Locate every blood parasite and identify its species.
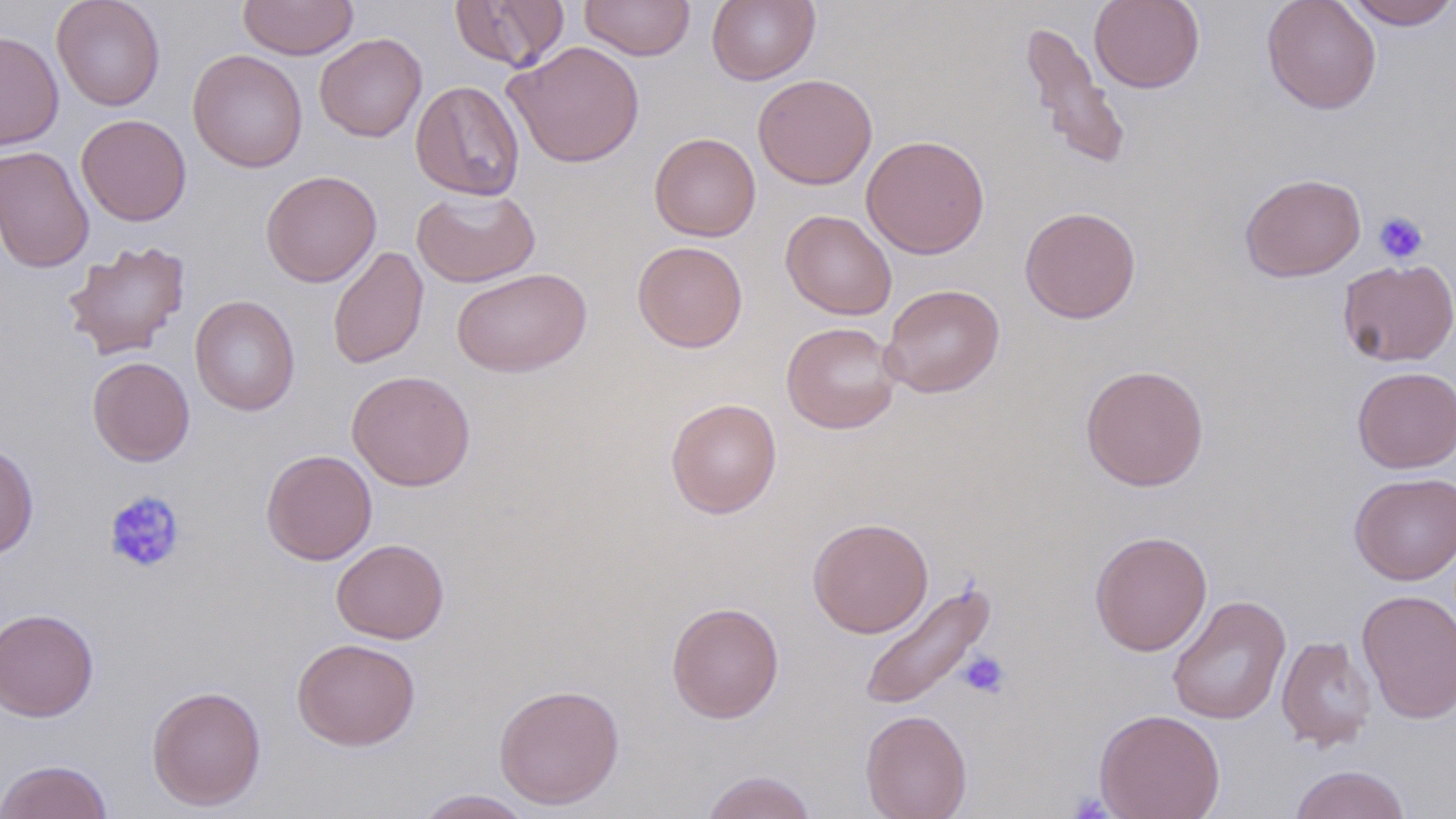
No blood parasites seen.

Summary:
  - Coordinate format: approximate bounding boxes as [x1, y1, x2, y2] in pixels
  - Platelet locations: [1373, 211, 1429, 264], [104, 490, 186, 574], [957, 650, 1011, 699], [1068, 791, 1116, 818]
  - Uninfected red blood cell locations: [51, 0, 166, 111], [238, 0, 358, 60], [449, 0, 571, 72], [579, 0, 695, 61], [706, 0, 820, 85], [1089, 0, 1205, 93], [1261, 0, 1382, 114], [1344, 0, 1456, 30], [1019, 20, 1132, 173], [0, 30, 64, 151], [314, 32, 427, 142], [505, 41, 645, 168], [187, 49, 307, 172], [752, 73, 877, 189], [410, 80, 525, 201], [76, 114, 192, 226], [649, 132, 761, 242], [861, 135, 989, 259], [0, 145, 94, 273], [260, 170, 381, 287], [1239, 173, 1366, 282], [411, 186, 541, 288], [1019, 206, 1141, 324], [781, 209, 897, 320], [62, 240, 191, 361], [632, 240, 748, 352], [328, 247, 429, 370], [1338, 258, 1456, 366], [452, 268, 591, 378], [880, 284, 1005, 398], [189, 295, 301, 416], [781, 321, 902, 434], [87, 356, 195, 466], [1080, 363, 1209, 491], [1352, 366, 1456, 473], [346, 370, 476, 491], [665, 396, 782, 519], [0, 441, 39, 559], [261, 449, 377, 565], [1349, 472, 1456, 585], [807, 517, 933, 638], [1089, 530, 1212, 656], [331, 539, 449, 644], [858, 578, 998, 712], [1357, 588, 1456, 725], [1167, 594, 1291, 725], [666, 601, 785, 724], [0, 608, 100, 722], [1276, 635, 1376, 753], [291, 637, 421, 751], [494, 683, 625, 810], [146, 685, 267, 811], [1094, 708, 1226, 819], [860, 709, 973, 819], [0, 758, 115, 819], [1289, 764, 1412, 819], [699, 770, 818, 819], [415, 789, 535, 818]
  - Slide-level diagnosis: negative for blood parasites
  - Stain: May-Grünwald-Giemsa
  - Image size: 1456×819 pixels
  - Preparation: thin blood film
  - Field of view: one of a larger specimen
  - Magnification: 1000x
  - Modality: optical microscopy